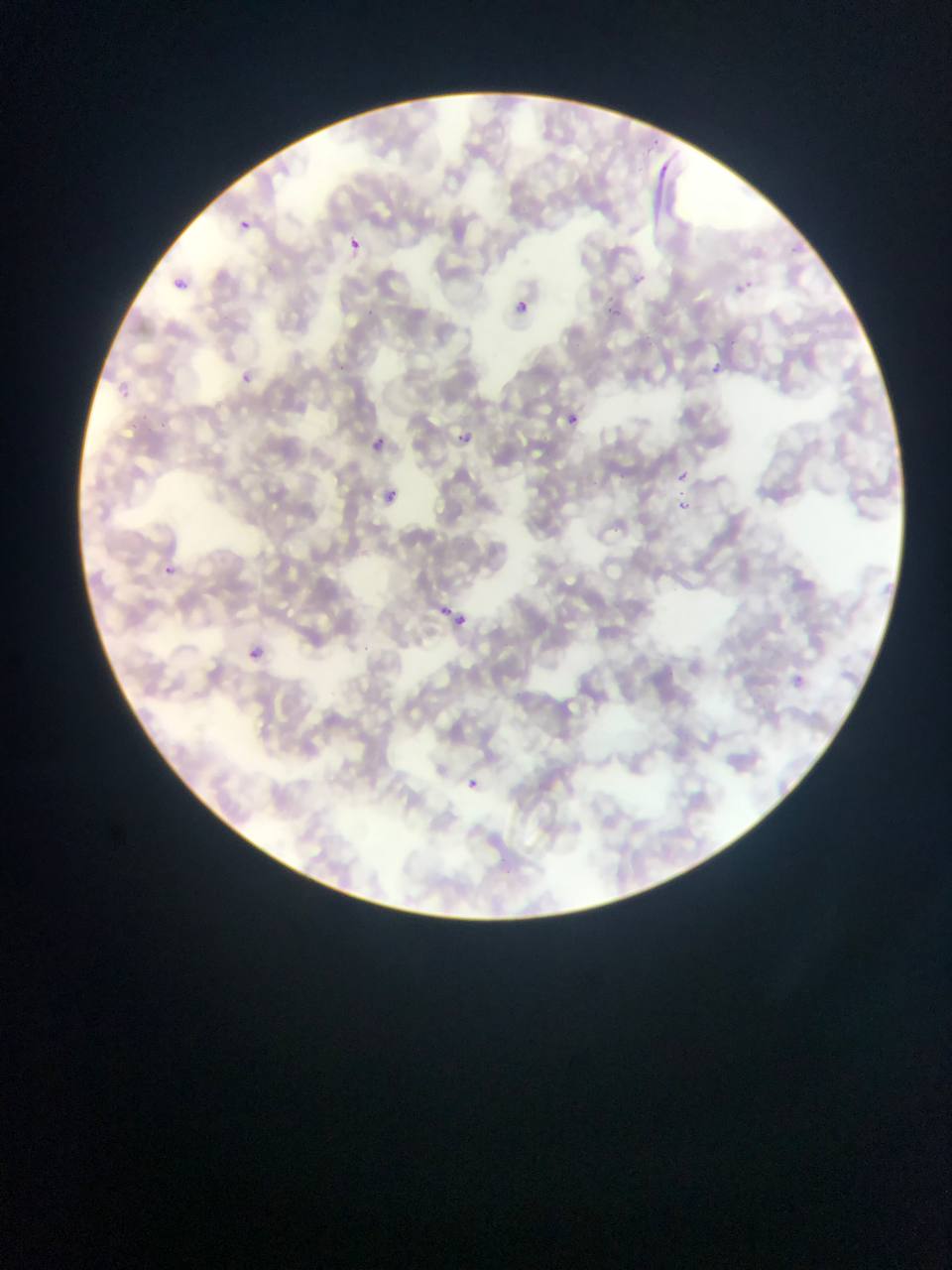

{
  "malaria_parasite_locations": "approximate bounding boxes as left top right bottom in pixels: 233 217 255 237; 345 237 363 255; 784 244 796 265; 170 268 191 284; 632 273 646 287; 727 274 760 301; 509 295 533 318; 605 298 629 326; 711 361 739 391; 237 372 254 380; 116 380 136 394; 564 412 581 428; 450 427 476 449; 367 434 388 455; 674 468 690 482; 381 485 401 505; 675 500 689 513; 154 559 183 585; 430 599 467 630; 245 646 264 663; 788 671 809 691; 462 775 485 794; 466 778 480 791",
  "preparation": "thin blood smear",
  "country": "Ghana",
  "image_size": "952×1270 pixels",
  "capture": "mobile-phone photograph through a microscope",
  "field_of_view": "single"
}